State which parasite is depicted.
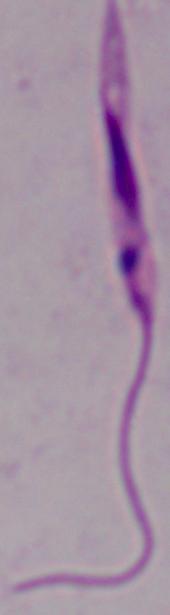
This is Leishmania.

Photomicrograph. Captured at 1000x magnification.